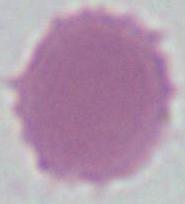

Micrograph. 1000x magnification. A red blood cell is seen.